Give the position of every Plasmodium parasite and every leukocyte.
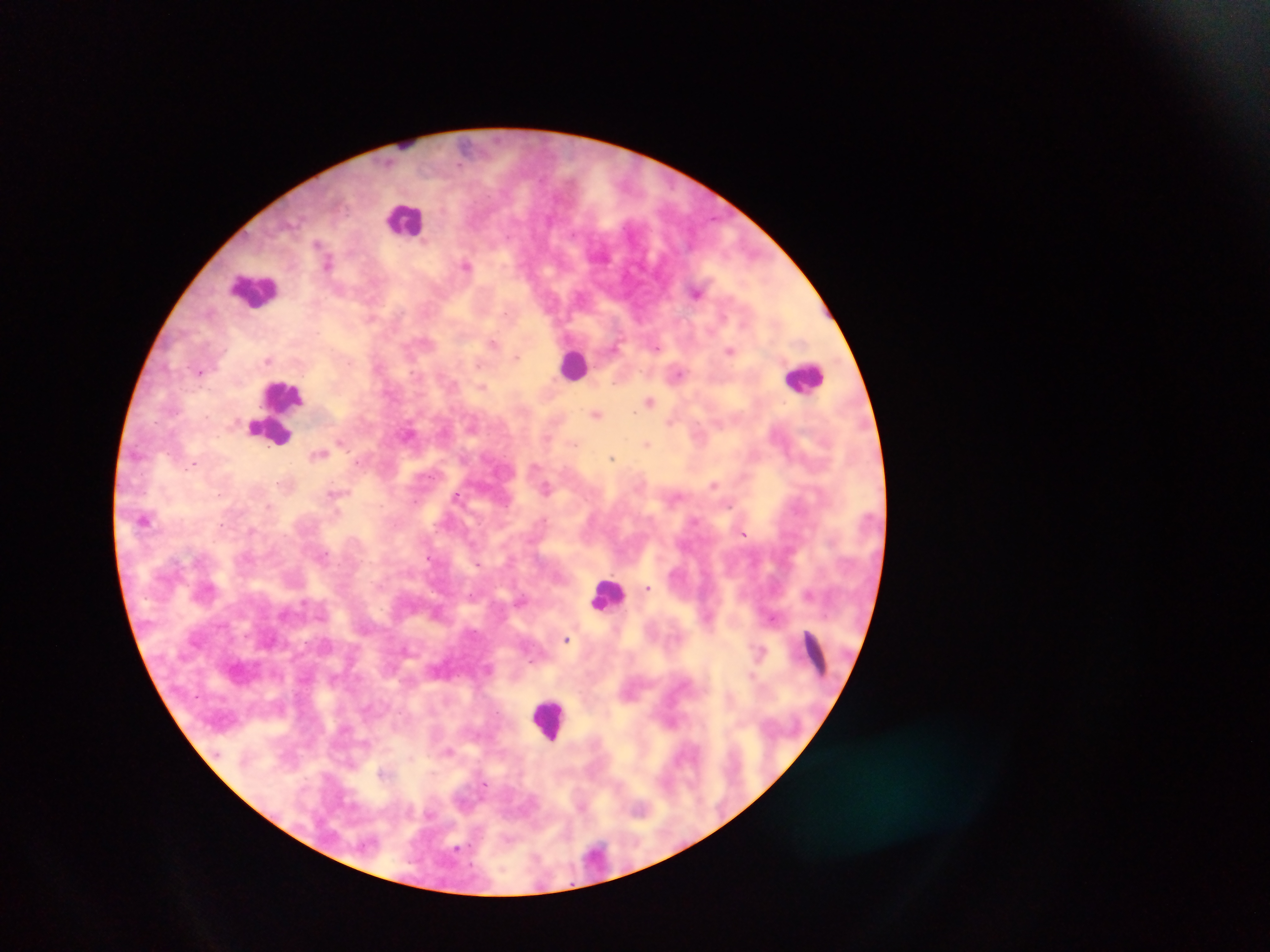
Approximate centers as (x, y) in pixels.
Plasmodium parasites: (328, 263), (466, 264), (696, 292), (493, 342), (615, 346), (730, 350), (517, 357), (268, 360), (200, 371), (678, 373), (483, 386), (650, 400), (597, 413), (671, 421), (410, 433), (341, 440), (647, 444), (319, 453), (612, 457), (195, 463), (715, 484), (546, 487), (333, 492), (219, 495), (457, 496), (145, 519), (252, 530), (743, 534), (648, 588), (809, 593), (773, 617), (566, 638), (759, 650), (752, 674), (449, 751).
Leukocytes: (405, 219), (255, 289), (575, 364), (805, 377), (276, 410), (608, 595), (816, 656), (549, 719).

Summary:
  - Image size: 1270×952 pixels
  - Country: Ghana
  - Capture: mobile-phone photograph through a microscope
  - Preparation: thick blood smear
  - Field of view: single